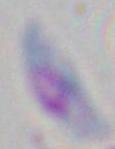
Summary:
  - Magnification: 1000x
  - Identification: Toxoplasma gondii
  - Modality: photomicrograph